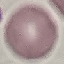

Summary:
  - Malaria status: uninfected
  - Capture: smartphone through the microscope eyepiece
  - Preparation: thin blood film
  - Image type: automatically extracted cell patch, resized to 64 × 64 pixels
  - Stain: Giemsa